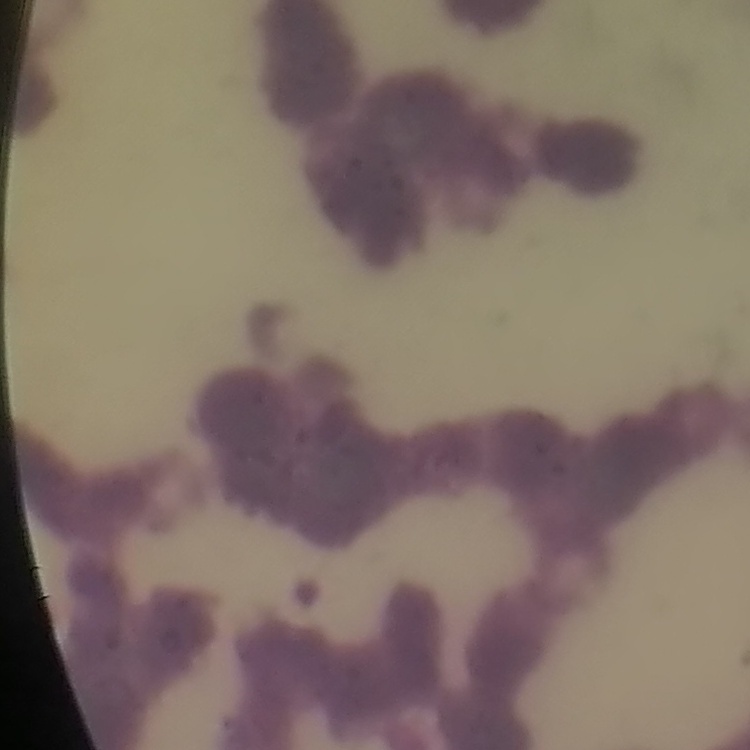
erythrocyte morphology = rouleaux formation
preparation = thin peripheral smear
stain = Field's or Giemsa
image type = one tile cut from a larger photomicrograph